Assess this cell for malaria.
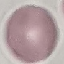
Uninfected.

Cell patch, automatically extracted from a larger field of view and resized to 64 × 64 pixels. Thin smear of blood. Giemsa stain. Photographed with a smartphone camera at the microscope eyepiece.